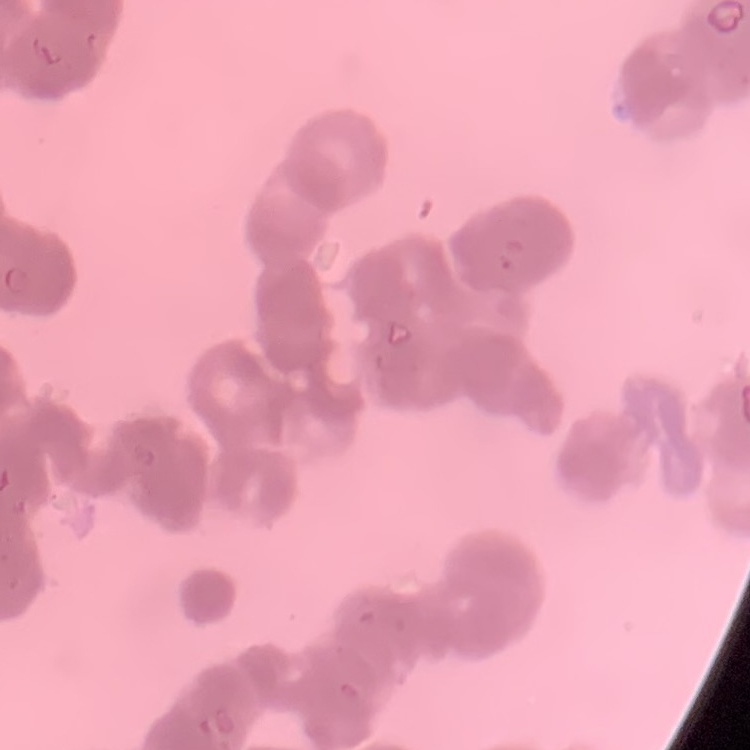

Summary:
  - Red blood cell morphology: rouleaux formation
  - Stain: Field's or Giemsa
  - Preparation: thin peripheral smear
  - Image type: square crop of a larger photomicrograph